State which parasite is depicted.
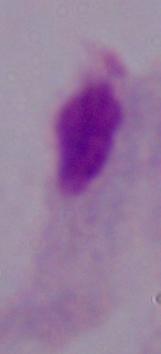
This is a trichomonad.

Summary:
  - Modality: micrograph
  - Magnification: 1000x